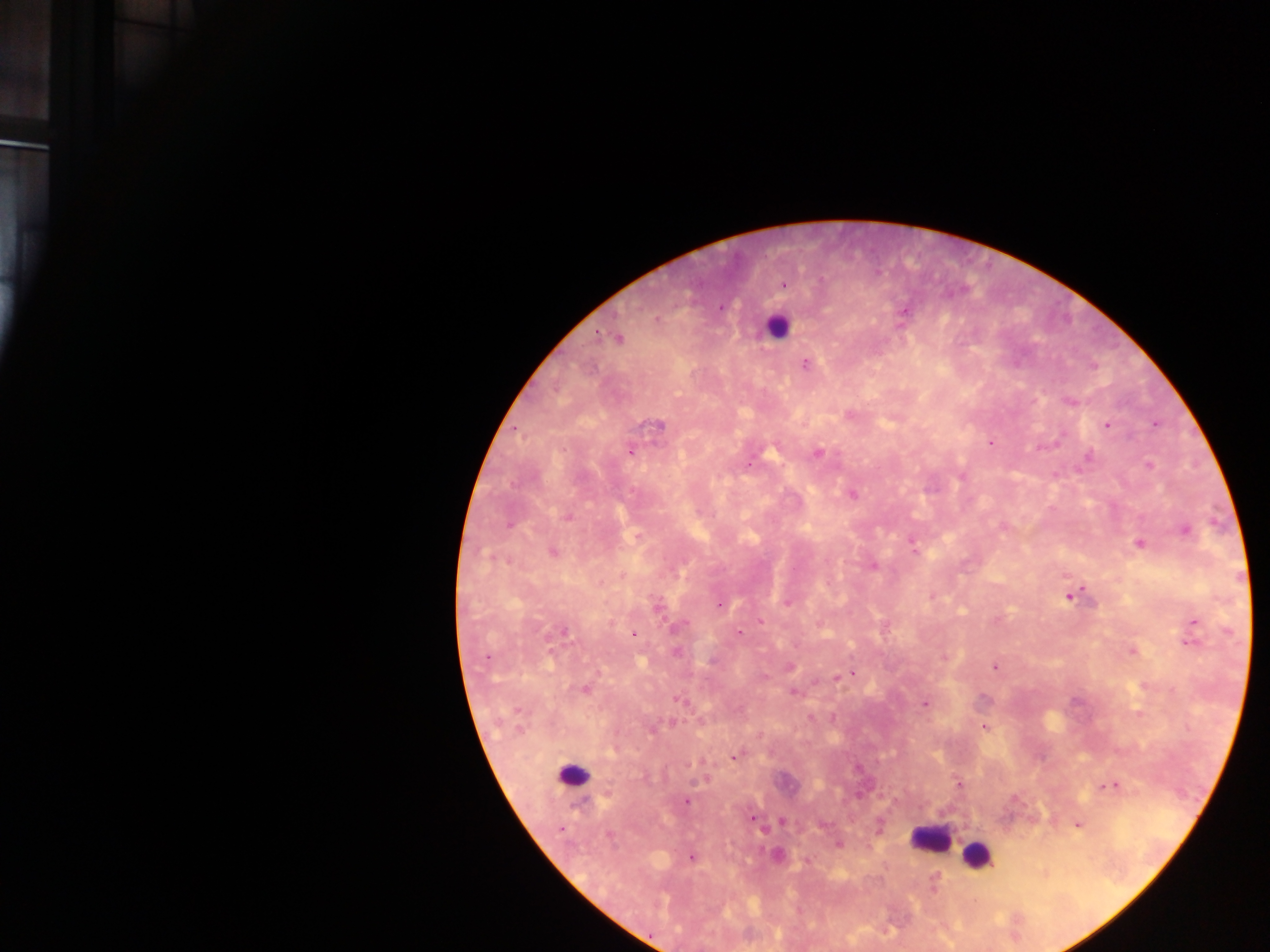
Approximate centers as (x, y) in pixels.
Summary:
  - Leukocyte locations: (775, 327), (574, 775), (929, 839), (977, 855)
  - Plasmodium parasite locations: (784, 284), (721, 307), (905, 311), (657, 319), (598, 335), (618, 338), (805, 364), (1070, 402), (850, 414), (1155, 423), (657, 425), (1107, 425), (990, 442), (630, 451), (818, 453), (1088, 458), (1149, 465), (962, 476), (852, 495), (568, 517), (509, 525), (1002, 527), (1185, 530), (912, 541), (1138, 543), (553, 552), (874, 567), (931, 596), (1068, 596), (787, 603), (718, 604), (657, 608), (760, 621), (1194, 622), (678, 626), (564, 633), (739, 633), (634, 635), (1191, 642), (1132, 651), (675, 652), (486, 657), (944, 658), (790, 667), (994, 667), (852, 673), (837, 676), (764, 677), (585, 689), (793, 692), (678, 698), (924, 704), (1138, 713), (832, 719), (672, 723), (984, 728), (653, 729), (735, 757), (704, 780), (958, 784), (1110, 785), (686, 801), (752, 819), (782, 821), (1078, 825), (560, 829), (763, 830), (609, 835), (838, 845), (777, 855), (691, 858), (934, 885)
  - Country: Ghana
  - Preparation: thick blood smear
  - Image size: 1270×952 pixels
  - Field of view: single
  - Capture: mobile-phone photograph through a microscope